Classify this cell by malaria status.
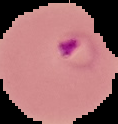

It is parasitized.

Summary:
  - Preparation: thin blood film
  - Image size: 118×124 pixels
  - Image type: segmented cell region with the area outside set to black